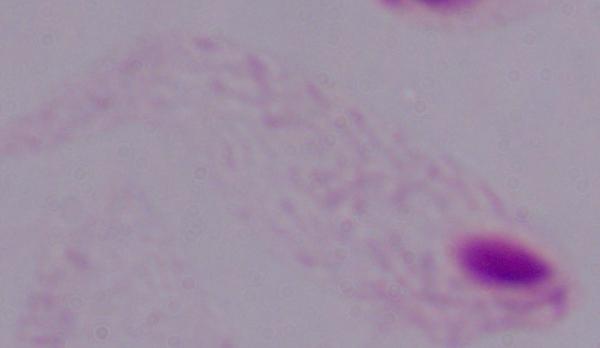

identification = trichomonad
magnification = 1000x
modality = micrograph